Classify this cell by malaria status.
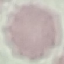
Uninfected.

Thin blood smear. Cell patch, automatically extracted from a larger field of view and resized to 64 × 64 pixels. Giemsa stain. Photographed with a smartphone camera at the microscope eyepiece.